Outline each blood parasite and name the species.
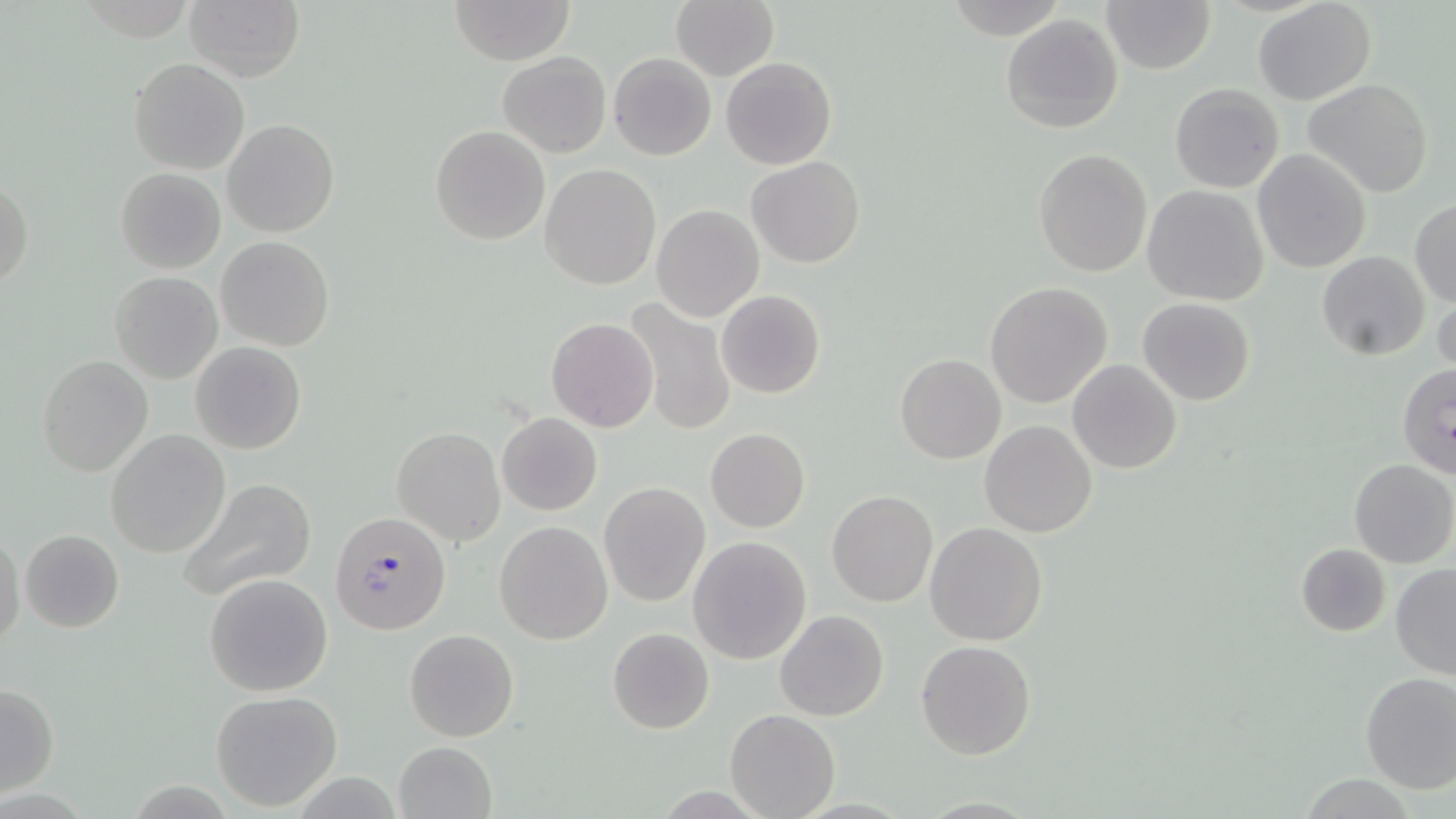

Approximate bounding boxes as named x1/y1/x2/y2 corners in pixels.
Plasmodium falciparum-infected red blood cells: (x1=329, y1=511, x2=451, y2=635).
No Plasmodium ovale, Plasmodium malariae, Plasmodium vivax, Babesia divergens, or Trypanosoma brucei observed.

{
  "slide_level_diagnosis": "Plasmodium falciparum",
  "preparation": "thin blood smear",
  "uninfected_red_blood_cell_locations": "approximate bounding boxes as named x1/y1/x2/y2 corners in pixels: (x1=183, y1=0, x2=304, y2=82), (x1=450, y1=0, x2=575, y2=65), (x1=670, y1=0, x2=778, y2=80), (x1=1253, y1=0, x2=1376, y2=106), (x1=1103, y1=1, x2=1214, y2=74), (x1=1000, y1=13, x2=1124, y2=133), (x1=498, y1=51, x2=612, y2=158), (x1=608, y1=52, x2=717, y2=160), (x1=721, y1=56, x2=837, y2=169), (x1=129, y1=57, x2=251, y2=174), (x1=1304, y1=78, x2=1434, y2=200), (x1=1170, y1=84, x2=1284, y2=194), (x1=223, y1=119, x2=340, y2=238), (x1=428, y1=125, x2=550, y2=246), (x1=1034, y1=148, x2=1152, y2=278), (x1=1252, y1=149, x2=1371, y2=273), (x1=747, y1=157, x2=865, y2=269), (x1=540, y1=165, x2=660, y2=290), (x1=115, y1=168, x2=224, y2=274), (x1=0, y1=177, x2=32, y2=293), (x1=1142, y1=185, x2=1269, y2=307), (x1=1410, y1=197, x2=1455, y2=308), (x1=652, y1=205, x2=764, y2=321), (x1=215, y1=236, x2=336, y2=351), (x1=1317, y1=252, x2=1430, y2=360), (x1=109, y1=272, x2=223, y2=384), (x1=984, y1=282, x2=1113, y2=408), (x1=1432, y1=289, x2=1455, y2=379), (x1=715, y1=290, x2=826, y2=399), (x1=622, y1=297, x2=736, y2=436), (x1=1137, y1=297, x2=1255, y2=405), (x1=546, y1=318, x2=659, y2=431), (x1=190, y1=341, x2=306, y2=455), (x1=38, y1=354, x2=154, y2=476), (x1=895, y1=354, x2=1006, y2=464), (x1=1067, y1=359, x2=1181, y2=474), (x1=1396, y1=362, x2=1456, y2=481), (x1=497, y1=412, x2=603, y2=514), (x1=979, y1=421, x2=1097, y2=537), (x1=392, y1=427, x2=505, y2=546), (x1=704, y1=428, x2=811, y2=532), (x1=106, y1=430, x2=231, y2=558), (x1=1349, y1=459, x2=1456, y2=569), (x1=175, y1=477, x2=318, y2=604), (x1=599, y1=481, x2=710, y2=607), (x1=827, y1=491, x2=937, y2=606), (x1=494, y1=521, x2=612, y2=644), (x1=925, y1=521, x2=1049, y2=646), (x1=1, y1=529, x2=24, y2=652), (x1=20, y1=529, x2=124, y2=632), (x1=688, y1=536, x2=813, y2=665), (x1=1296, y1=543, x2=1390, y2=638), (x1=1390, y1=564, x2=1456, y2=679), (x1=204, y1=572, x2=332, y2=696), (x1=774, y1=610, x2=889, y2=722), (x1=607, y1=627, x2=714, y2=734), (x1=404, y1=629, x2=519, y2=742), (x1=916, y1=638, x2=1036, y2=760), (x1=1359, y1=671, x2=1456, y2=793), (x1=0, y1=684, x2=60, y2=795), (x1=210, y1=690, x2=343, y2=812), (x1=725, y1=709, x2=841, y2=819), (x1=393, y1=741, x2=498, y2=819)",
  "image_size": "1456×819 pixels",
  "magnification": "1000x",
  "field_of_view": "one of a larger specimen",
  "stain": "May-Grünwald-Giemsa",
  "modality": "light microscopy"
}